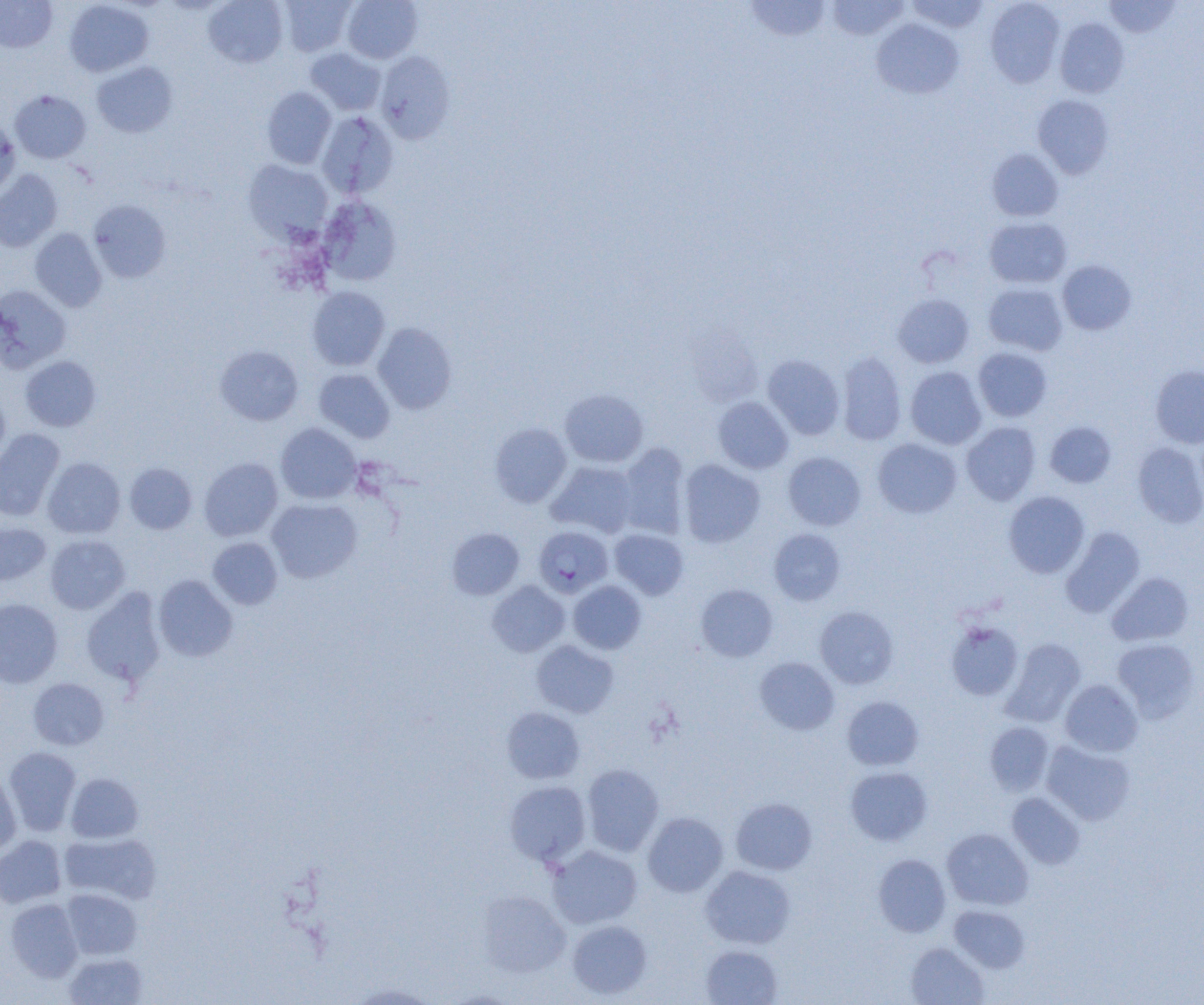
slide-level diagnosis = Plasmodium falciparum
uninfected red blood cell locations = approximate bounding boxes as (x1,y1)-(x2,y2) corner pairs in pixels: (203,0)-(288,68), (279,0)-(356,56), (341,0)-(423,63), (745,0)-(832,42), (905,0)-(990,33), (985,0)-(1064,88), (1103,0)-(1181,38), (0,1)-(57,53), (64,1)-(154,77), (827,1)-(909,40), (871,18)-(964,99), (1055,18)-(1128,97), (305,47)-(386,115), (375,50)-(455,144), (91,61)-(177,137), (261,87)-(336,169), (10,90)-(91,163), (1032,94)-(1115,179), (317,111)-(398,199), (0,117)-(20,199), (987,149)-(1064,221), (243,160)-(334,243), (0,169)-(62,252), (318,195)-(402,286), (88,199)-(171,283), (983,216)-(1072,289), (30,229)-(107,311), (1058,259)-(1136,335), (983,282)-(1068,355), (0,284)-(71,372), (307,286)-(390,371), (892,293)-(975,368), (373,322)-(457,414), (215,345)-(303,425), (973,347)-(1052,422), (836,351)-(907,446), (763,355)-(845,440), (21,356)-(101,431), (1150,365)-(1204,448), (905,366)-(986,449), (314,368)-(395,442), (560,389)-(648,468), (0,391)-(10,468), (712,396)-(793,474), (1045,421)-(1116,488), (490,422)-(571,507), (961,422)-(1041,505), (275,423)-(361,504), (0,428)-(65,520), (873,438)-(961,518), (1133,443)-(1204,527), (617,444)-(689,539), (783,452)-(866,530), (42,457)-(126,539), (199,457)-(283,541), (678,459)-(765,547), (547,461)-(638,538), (124,463)-(197,534), (1003,491)-(1089,578), (266,499)-(362,583), (0,521)-(51,587), (1060,526)-(1145,618), (447,528)-(524,600), (769,528)-(845,606), (609,529)-(689,600), (45,534)-(130,614), (208,537)-(283,610), (1107,572)-(1193,646), (154,575)-(237,662), (487,580)-(570,656), (568,580)-(646,654), (695,583)-(778,662), (81,588)-(166,688), (0,598)-(62,688), (815,606)-(899,689), (945,620)-(1024,700), (1000,638)-(1086,727), (1112,638)-(1200,721), (531,640)-(619,718), (755,656)-(840,735), (28,678)-(110,750), (1060,679)-(1143,757), (842,696)-(924,770), (501,707)-(585,784), (985,722)-(1054,795), (1041,740)-(1135,825), (3,747)-(81,836), (581,764)-(664,856), (845,766)-(932,846), (0,771)-(21,855), (65,772)-(144,843), (504,780)-(591,866), (1007,792)-(1085,869), (731,797)-(817,875), (642,813)-(728,897), (941,828)-(1033,910), (59,832)-(161,904), (0,835)-(66,908), (547,845)-(642,929), (873,854)-(951,937), (700,865)-(795,949), (61,889)-(142,960), (478,891)-(571,978), (5,898)-(84,982), (949,905)-(1030,973), (568,920)-(653,999), (906,942)-(989,1004), (700,945)-(782,1005), (63,952)-(148,1005), (346,981)-(438,1004)
modality = light microscopy
Plasmodium falciparum-infected red blood cell locations = approximate bounding boxes as (x1,y1)-(x2,y2) corner pairs in pixels: (534,526)-(613,598)
magnification = 1000x
image size = 1204×1005 pixels
preparation = thin blood smear
field of view = single